Name the parasite shown.
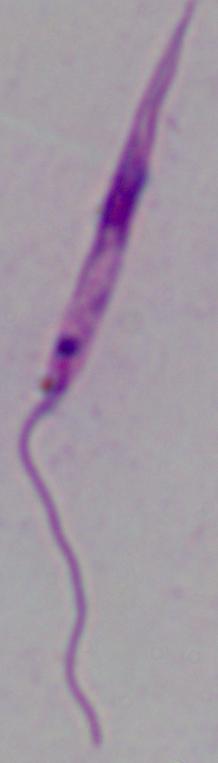

Leishmania.

Summary:
  - Magnification: 1000x
  - Modality: photomicrograph